Locate every blood parasite and identify its species.
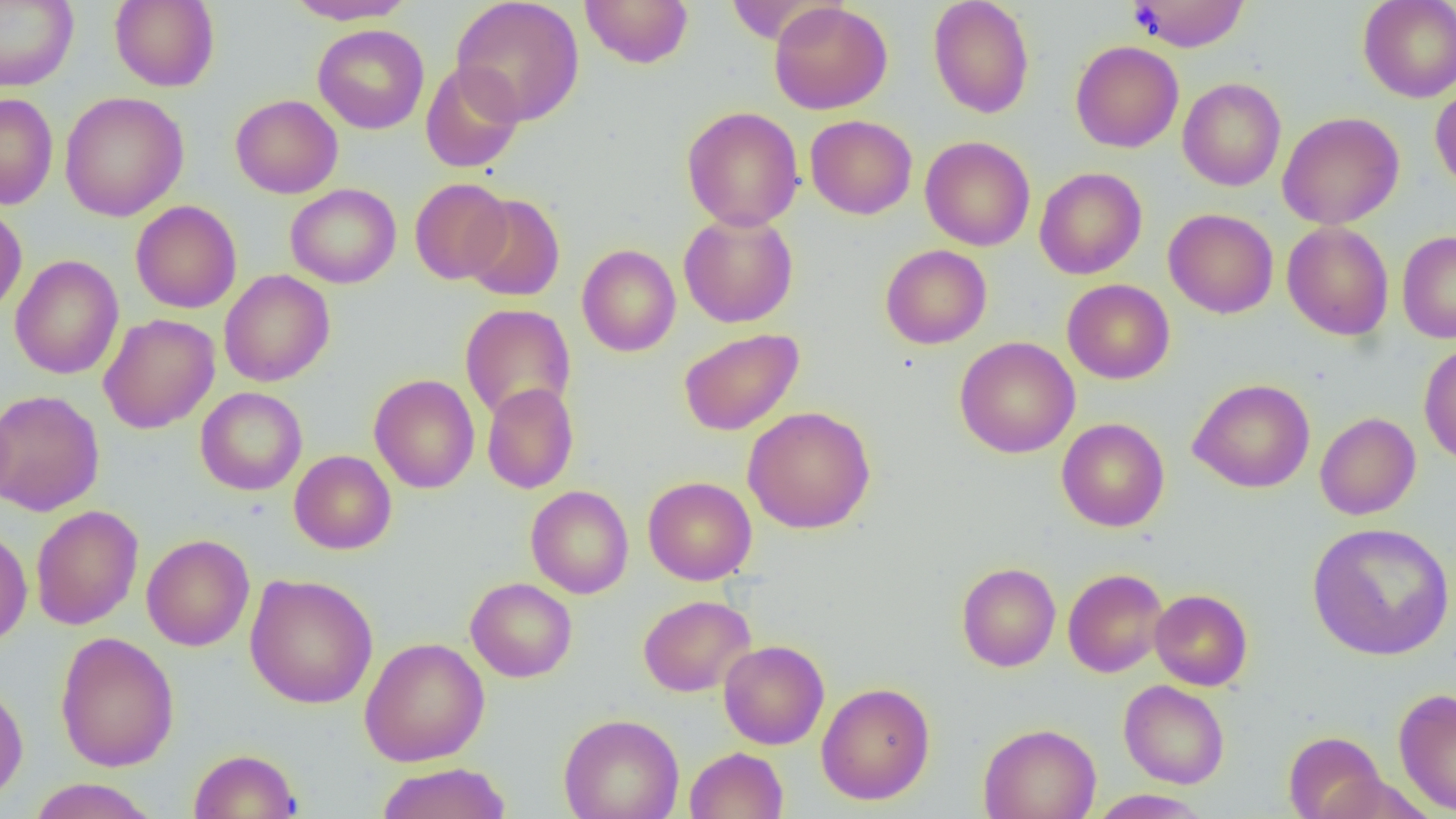

No blood parasites observed.

slide-level diagnosis = negative for blood parasites
magnification = 1000x
field of view = one of a larger specimen
modality = light microscopy
uninfected red blood cell locations = approximate bounding boxes as (x1,y1)-(x2,y2) corner pairs in pixels: (110,0)-(220,91), (284,0)-(417,25), (451,0)-(585,126), (580,0)-(694,69), (928,0)-(1035,118), (1128,0)-(1251,52), (1358,0)-(1456,102), (0,1)-(78,91), (769,2)-(893,115), (313,24)-(429,134), (1070,40)-(1184,153), (420,62)-(524,173), (1178,77)-(1286,191), (1430,82)-(1456,195), (59,91)-(189,222), (0,93)-(58,209), (230,94)-(343,198), (681,106)-(804,230), (1277,112)-(1404,229), (805,115)-(917,219), (920,136)-(1035,251), (1034,166)-(1147,280), (410,178)-(512,284), (285,183)-(401,288), (461,194)-(565,301), (131,200)-(242,313), (0,203)-(27,318), (1163,208)-(1278,318), (678,212)-(798,328), (1282,221)-(1394,340), (1397,231)-(1456,343), (577,244)-(681,357), (880,244)-(992,349), (9,254)-(124,380), (219,269)-(335,387), (1062,278)-(1175,384), (460,303)-(576,422), (98,313)-(220,434), (678,327)-(804,436), (955,336)-(1080,459), (1419,342)-(1456,466), (369,374)-(480,494), (1188,378)-(1315,493), (482,383)-(579,494), (196,387)-(308,495), (0,389)-(104,517), (743,406)-(876,533), (1315,412)-(1421,520), (1057,418)-(1170,532), (289,450)-(396,554), (643,476)-(757,585), (526,485)-(634,598), (30,504)-(144,630), (1306,521)-(1456,660), (0,525)-(32,650), (141,534)-(255,651), (956,562)-(1061,672), (1063,568)-(1168,678), (244,574)-(378,709), (465,577)-(577,682), (1150,589)-(1252,690), (638,594)-(755,697), (55,631)-(179,772), (360,637)-(489,766), (718,640)-(829,749), (0,679)-(29,805), (1118,680)-(1230,789), (817,682)-(935,805), (1393,689)-(1456,814), (559,713)-(684,819), (978,723)-(1101,819), (1284,730)-(1387,819), (685,747)-(788,819), (188,748)-(302,819), (375,761)-(512,819), (27,778)-(160,819), (1088,789)-(1213,818)
preparation = thin blood film
image size = 1456×819 pixels